Describe the morphology of the red blood cells.
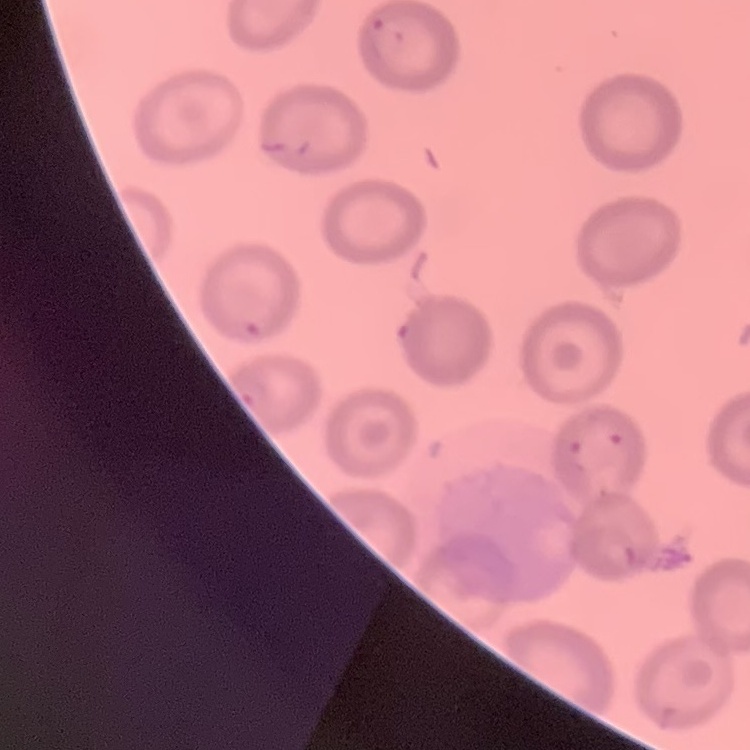
No rouleaux formation.

Summary:
  - Image type: one tile cut from a larger photomicrograph
  - Stain: Field's or Giemsa
  - Preparation: thin blood smear